Locate every Plasmodium falciparum-infected red blood cell.
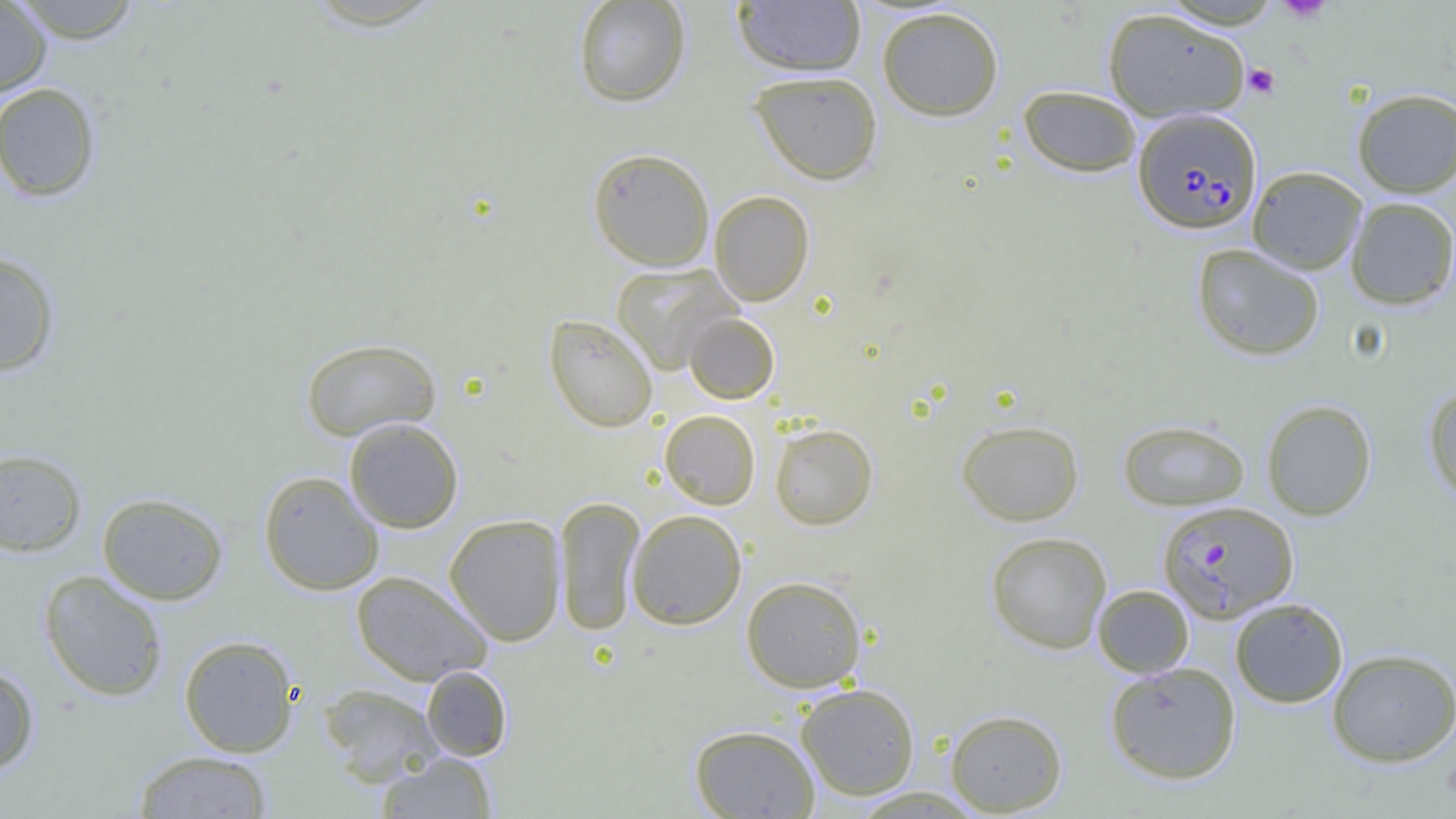

Approximate bounding boxes as (x1, y1, x2, y2) in pixels.
Plasmodium falciparum-infected red blood cells: (1132, 108, 1261, 234), (1157, 501, 1298, 623).

Summary:
  - Platelet locations: (1275, 0, 1333, 22), (1243, 64, 1280, 99)
  - Uninfected red blood cell locations: (10, 0, 143, 43), (572, 0, 692, 108), (0, 1, 52, 97), (732, 1, 866, 76), (876, 6, 1004, 121), (1102, 8, 1250, 122), (748, 70, 884, 185), (0, 82, 101, 202), (1017, 84, 1142, 177), (1352, 88, 1456, 197), (587, 147, 715, 271), (1247, 166, 1367, 274), (709, 190, 814, 306), (1345, 196, 1456, 309), (1192, 243, 1325, 360), (0, 251, 61, 376), (611, 263, 741, 374), (683, 312, 780, 404), (544, 314, 658, 433), (300, 337, 442, 442), (1423, 385, 1456, 505), (1261, 399, 1377, 521), (659, 409, 761, 510), (343, 417, 464, 534), (956, 419, 1084, 526), (1117, 419, 1250, 511), (769, 423, 878, 530), (0, 448, 87, 556), (258, 471, 384, 596), (97, 492, 228, 605), (553, 496, 644, 636), (627, 509, 747, 630), (444, 514, 567, 646), (985, 531, 1112, 653), (351, 569, 492, 685), (39, 570, 169, 701), (741, 575, 867, 693), (1092, 585, 1194, 678), (1229, 597, 1349, 708), (178, 635, 300, 757), (1326, 647, 1456, 767), (1104, 661, 1242, 785), (0, 663, 41, 775), (421, 665, 513, 761), (318, 683, 445, 784), (795, 683, 921, 800), (944, 709, 1067, 815), (689, 724, 820, 818), (133, 750, 273, 818), (376, 752, 498, 818)
  - Slide-level diagnosis: Plasmodium falciparum
  - Image size: 1456×819 pixels
  - Modality: light microscopy
  - Preparation: thin blood smear
  - Field of view: single
  - Magnification: 1000x